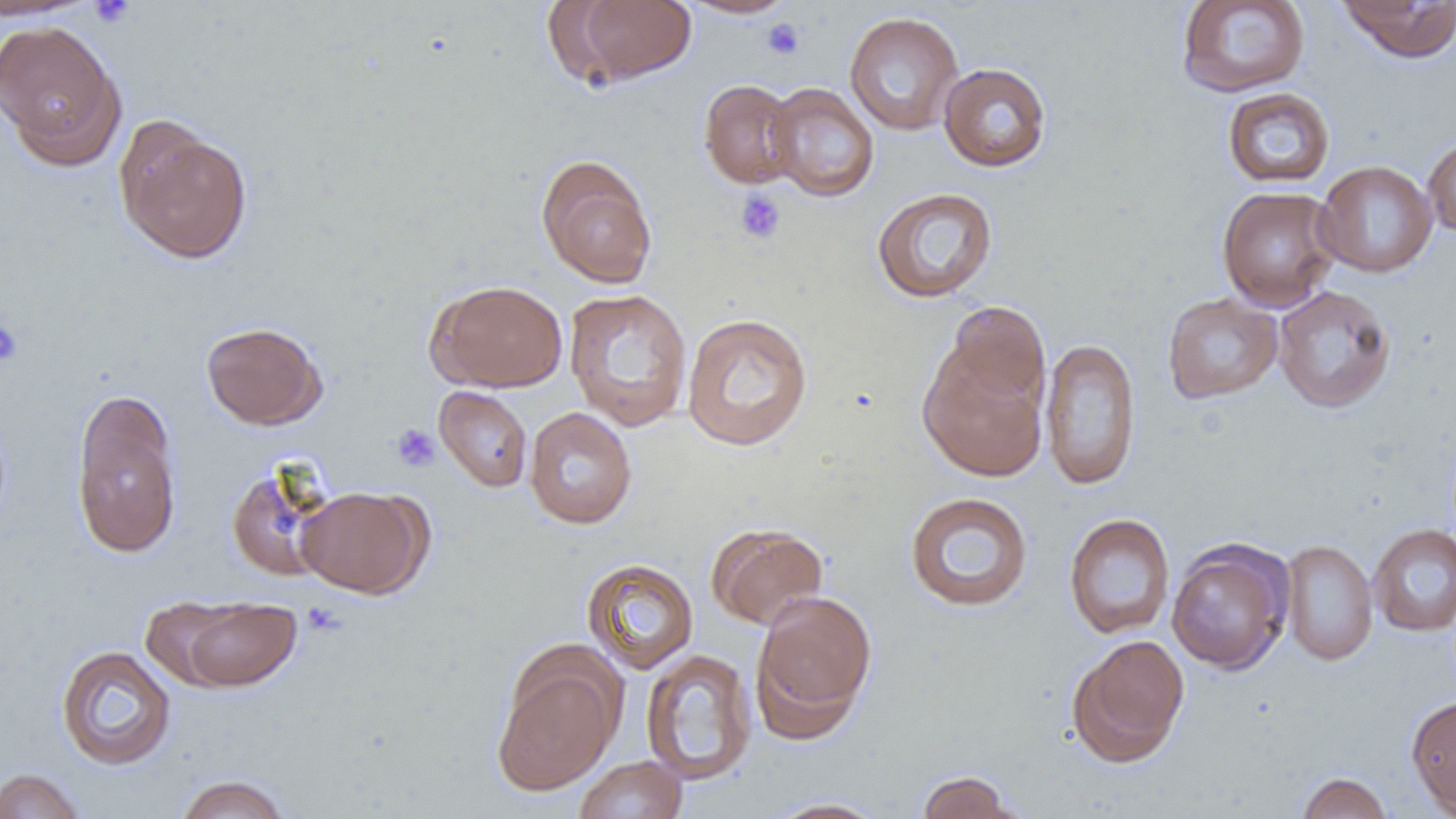

slide-level diagnosis = negative for blood parasites
uninfected red blood cell locations = approximate bounding boxes as [x1, y1, x2, y2] in pixels: [0, 0, 97, 21], [560, 0, 697, 86], [679, 0, 798, 19], [1175, 0, 1311, 98], [1337, 0, 1455, 63], [844, 12, 963, 136], [0, 20, 126, 168], [937, 62, 1052, 172], [698, 79, 802, 188], [766, 82, 880, 201], [1221, 87, 1336, 188], [116, 121, 252, 265], [1422, 134, 1456, 238], [536, 155, 658, 289], [1314, 160, 1437, 278], [1216, 186, 1341, 311], [871, 187, 998, 303], [427, 279, 568, 393], [1273, 285, 1396, 413], [563, 288, 693, 432], [1162, 292, 1283, 404], [942, 302, 1051, 414], [681, 312, 814, 452], [200, 321, 328, 430], [1039, 337, 1141, 491], [918, 345, 1048, 481], [434, 386, 533, 492], [70, 391, 183, 558], [524, 407, 637, 529], [225, 462, 340, 582], [296, 486, 431, 598], [904, 491, 1035, 612], [1063, 512, 1176, 640], [707, 523, 829, 631], [1368, 524, 1456, 637], [1166, 538, 1294, 675], [1280, 539, 1377, 665], [581, 558, 699, 674], [750, 591, 878, 738], [139, 596, 244, 690], [177, 597, 302, 692], [1066, 635, 1190, 767], [56, 644, 177, 770], [641, 647, 757, 786], [492, 653, 623, 797], [1405, 694, 1456, 816], [574, 756, 688, 819], [0, 768, 86, 819], [914, 770, 1024, 819], [1294, 771, 1393, 818], [174, 774, 293, 819], [765, 798, 890, 818]
magnification = 1000x
field of view = one of a larger specimen
image size = 1456×819 pixels
platelet locations = approximate bounding boxes as [x1, y1, x2, y2] in pixels: [88, 0, 135, 28], [761, 17, 805, 60], [734, 189, 787, 244], [0, 318, 24, 368], [391, 423, 441, 472], [301, 601, 348, 638]
modality = light microscopy
preparation = thin blood film